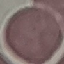

Result: negative for malaria parasites. Giemsa stain. Photographed with a smartphone camera at the microscope eyepiece. Cell patch, automatically extracted from a larger field of view and resized to 64 × 64 pixels. Thin blood film.